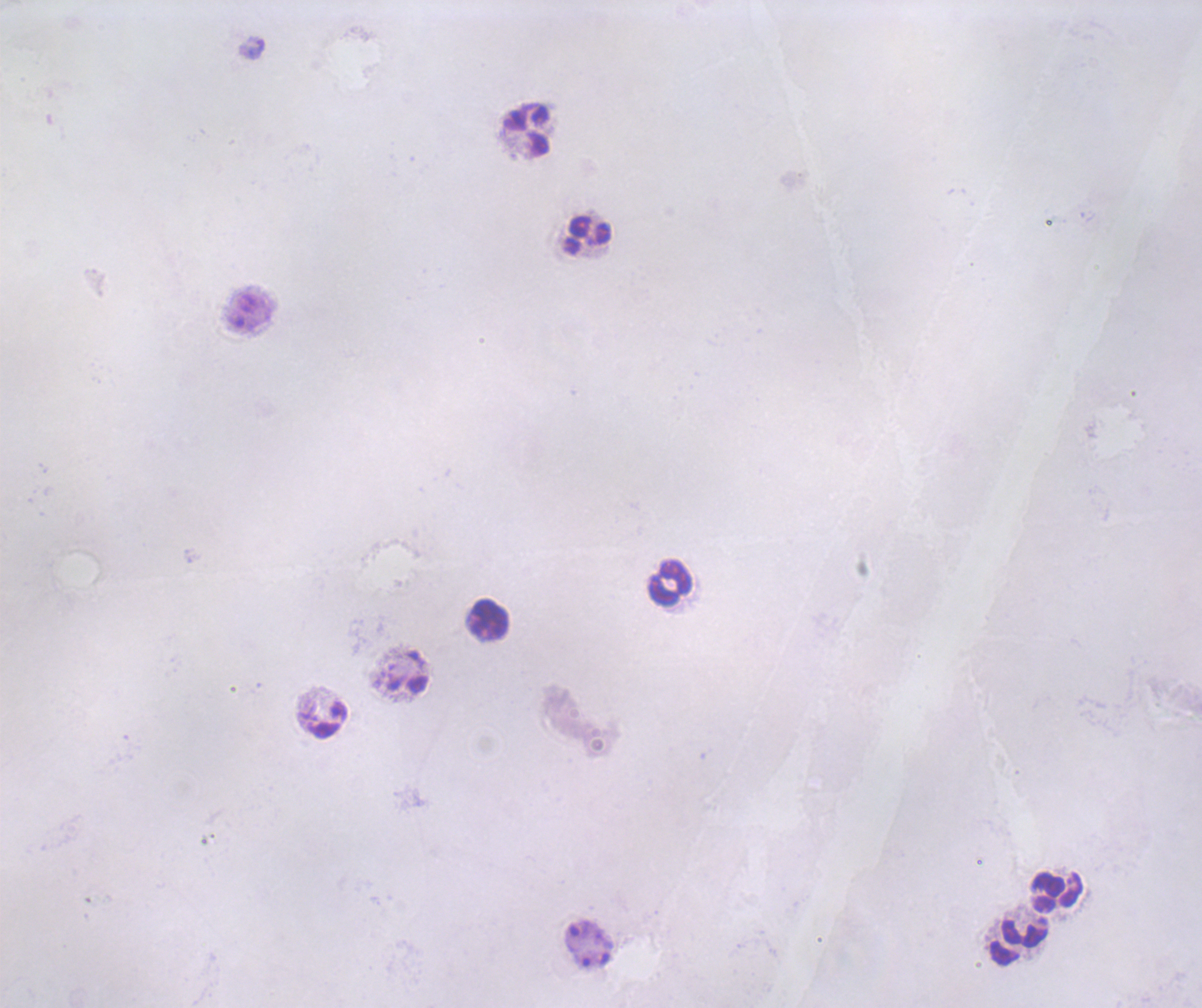

Approximate object centers, in pixels from the top-left corner.
Summary:
  - Leukocyte locations: (x=528, y=130), (x=587, y=235), (x=669, y=581), (x=488, y=619), (x=329, y=720), (x=1056, y=891), (x=1024, y=933)
  - Magnification: 100x
  - Stain: Romanowsky
  - Result: no malaria parasites seen
  - Field of view: one from this slide
  - Coloration quality: bad
  - Background quality: unsatisfactory
  - Preparation: thick blood smear
  - Image size: 1202×1008 pixels
  - Context: previously used in a real diagnosis